Comment on the morphology of the erythrocytes.
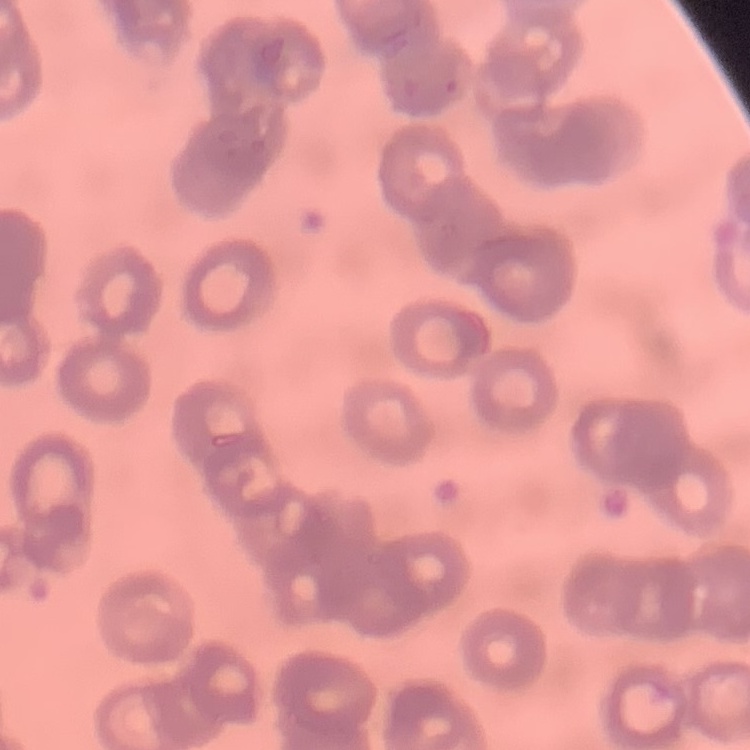
They show rouleaux formation.

{
  "image_type": "one tile cut from a larger photomicrograph",
  "preparation": "thin blood smear",
  "stain": "Field's or Giemsa"
}